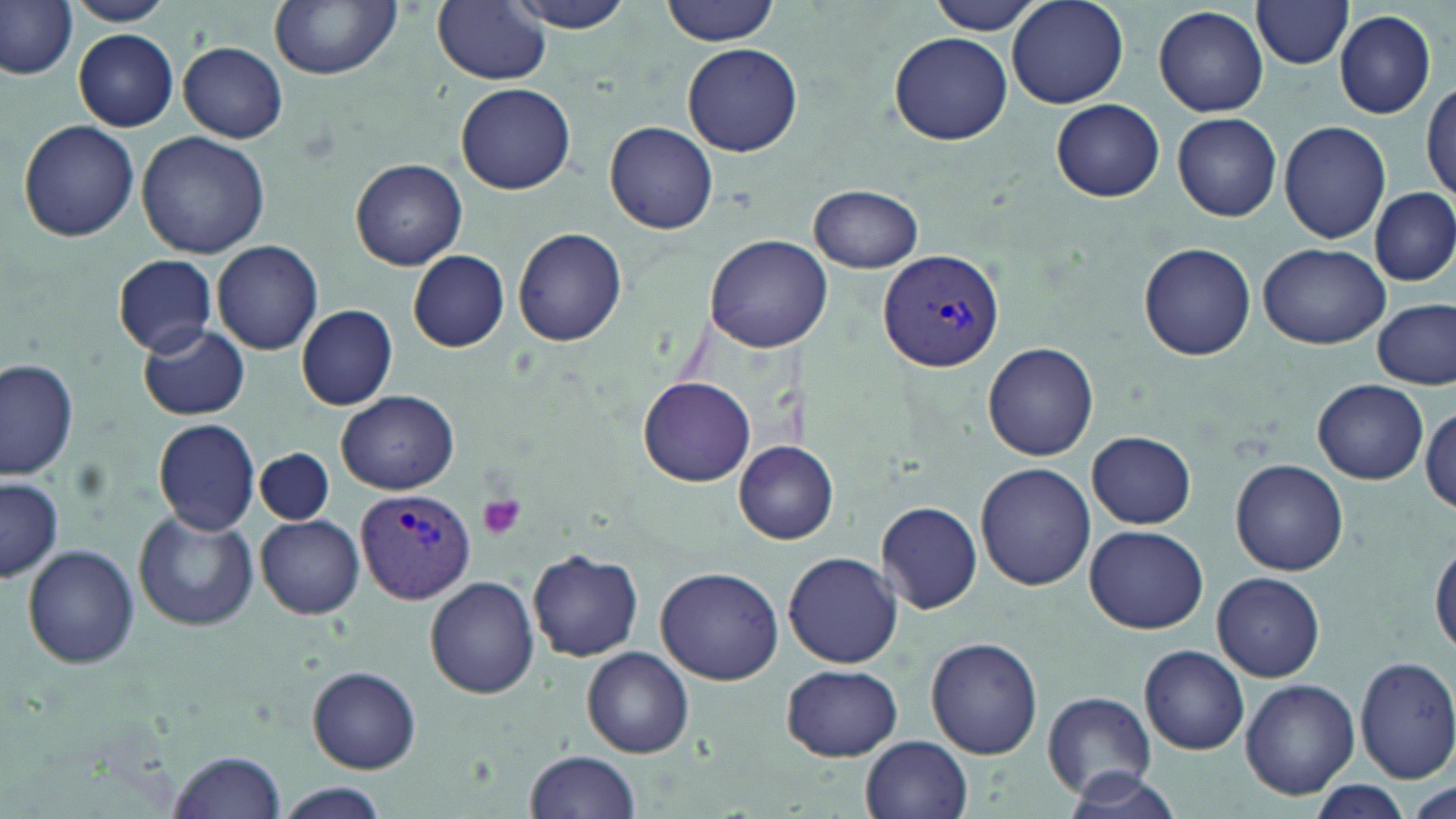
Summary:
  - Coordinate format: approximate bounding boxes as (x1, y1, x2, y2) in pixels
  - Plasmodium vivax-infected red blood cell locations: (877, 247, 1005, 373), (357, 489, 472, 604)
  - Platelet locations: (477, 493, 527, 540)
  - Uninfected red blood cell locations: (68, 0, 172, 26), (269, 0, 404, 79), (501, 0, 639, 33), (662, 0, 781, 45), (1006, 0, 1129, 107), (0, 1, 78, 82), (432, 1, 550, 85), (924, 1, 1048, 34), (1251, 1, 1356, 69), (1154, 5, 1268, 117), (1335, 9, 1438, 120), (74, 29, 179, 130), (889, 32, 1013, 146), (178, 41, 288, 143), (682, 43, 803, 157), (1422, 74, 1456, 207), (456, 83, 577, 195), (1050, 99, 1165, 202), (1172, 111, 1282, 221), (18, 120, 140, 243), (1279, 120, 1391, 244), (605, 122, 718, 235), (137, 131, 270, 258), (352, 159, 467, 270), (808, 184, 923, 272), (1371, 187, 1455, 287), (513, 227, 625, 348), (704, 235, 830, 352), (210, 240, 323, 355), (1140, 242, 1256, 359), (1258, 243, 1388, 349), (408, 251, 510, 351), (113, 254, 218, 355), (1373, 297, 1454, 389), (297, 305, 397, 410), (136, 322, 251, 420), (984, 343, 1100, 462), (0, 358, 78, 482), (638, 377, 755, 488), (1314, 380, 1428, 484), (335, 390, 458, 493), (1421, 399, 1454, 514), (152, 417, 261, 536), (1087, 432, 1196, 527), (734, 441, 839, 544), (256, 448, 333, 526), (1230, 460, 1348, 575), (975, 462, 1093, 590), (0, 477, 62, 581), (877, 501, 982, 613), (133, 510, 258, 632), (255, 515, 365, 618), (1085, 524, 1208, 634), (1431, 539, 1456, 659), (23, 544, 139, 668), (527, 548, 644, 661), (784, 551, 903, 668), (655, 564, 785, 683), (1211, 572, 1326, 680), (424, 577, 540, 699), (925, 637, 1043, 759), (1139, 644, 1249, 755), (583, 647, 695, 758), (1354, 655, 1456, 784), (781, 664, 902, 761), (308, 667, 421, 773), (1241, 678, 1359, 799), (1042, 692, 1154, 798), (860, 735, 972, 819), (169, 749, 286, 819), (524, 750, 641, 819), (1063, 770, 1184, 819), (272, 781, 390, 819), (1308, 782, 1414, 815)
  - Slide-level diagnosis: Plasmodium vivax
  - Magnification: 1000x
  - Preparation: thin blood smear
  - Stain: May-Grünwald-Giemsa
  - Image size: 1456×819 pixels
  - Modality: optical microscopy
  - Field of view: one of a larger specimen